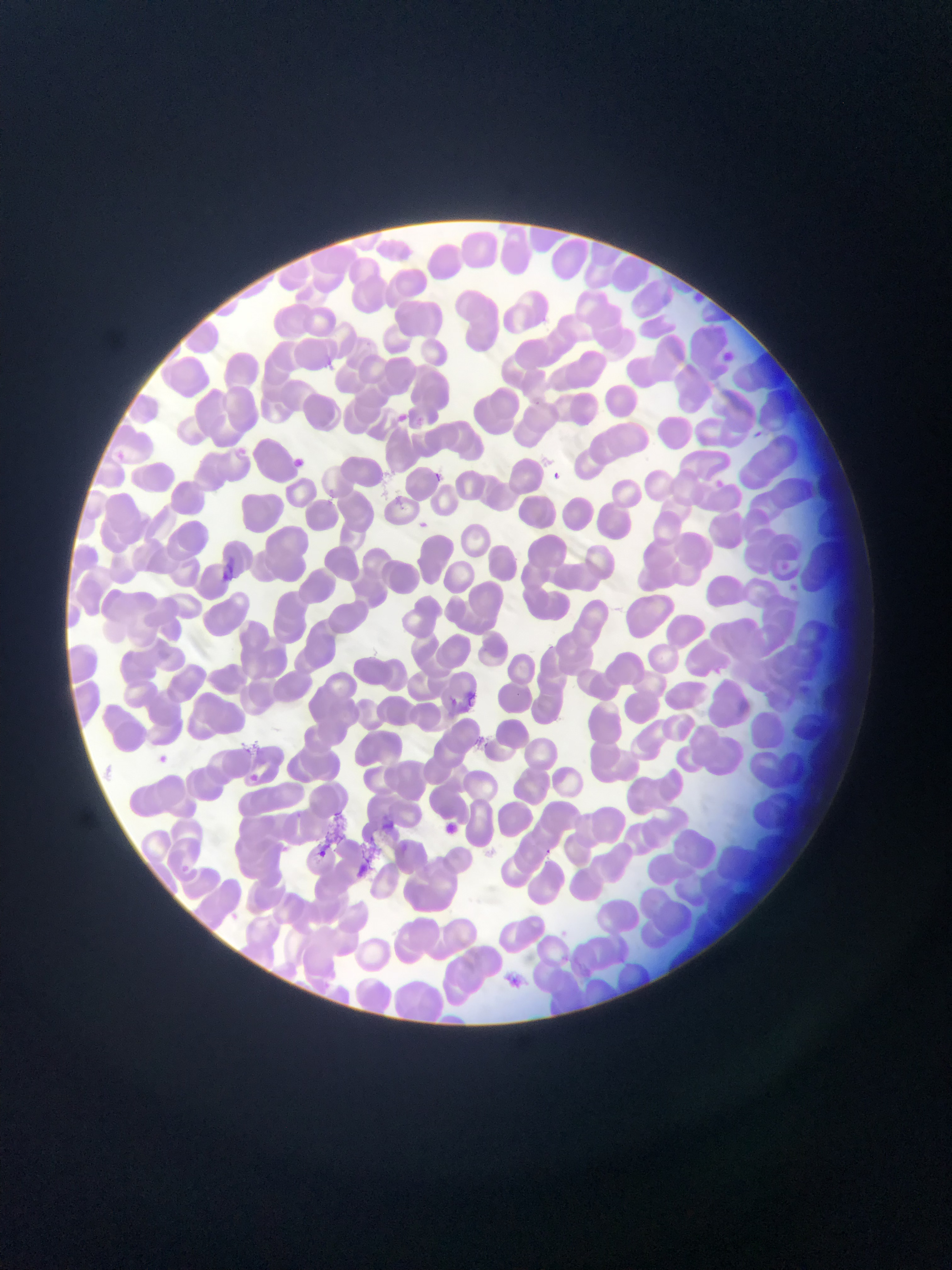
Approximate bounding boxes as left top right bottom in pixels. Plasmodium parasite locations: 720 347 740 367; 324 357 335 372; 397 411 417 432; 753 427 770 447; 292 448 303 472; 114 449 127 466; 549 462 569 495; 434 468 448 487; 712 475 724 494; 419 516 433 533; 777 557 793 575; 467 689 476 704; 446 691 463 714; 157 751 174 774; 244 768 266 795; 443 815 466 841; 311 842 328 856; 501 968 522 988. Sample from Ghana. Thin blood smear. Image is 952×1270 pixels. Single field of view. Mobile-phone photograph taken through the microscope.